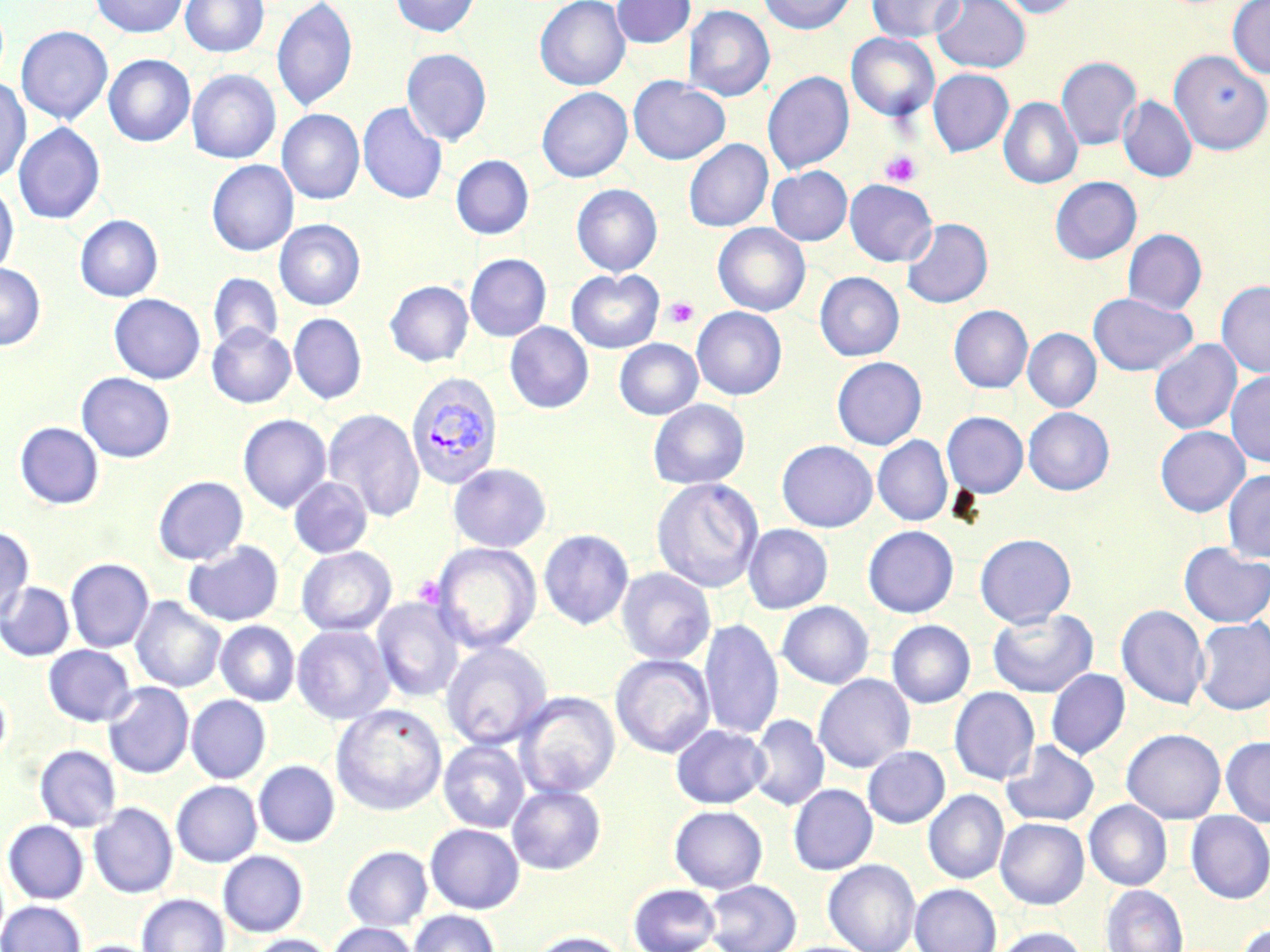

Summary:
  - Coordinate format: approximate bounding boxes as (x1, y1, x2, y2) in pixels
  - Uninfected red blood cell locations: (89, 0, 188, 37), (180, 0, 269, 57), (271, 0, 358, 113), (391, 0, 481, 37), (534, 0, 630, 90), (611, 0, 696, 48), (757, 0, 856, 34), (867, 0, 965, 43), (932, 0, 1031, 73), (996, 0, 1084, 18), (1227, 0, 1270, 78), (683, 5, 775, 102), (15, 25, 113, 124), (846, 32, 939, 121), (401, 48, 492, 146), (1170, 51, 1269, 155), (104, 54, 195, 146), (1056, 57, 1141, 150), (928, 68, 1014, 156), (188, 70, 280, 163), (195, 71, 287, 255), (762, 71, 854, 174), (0, 77, 31, 184), (628, 77, 730, 165), (536, 87, 632, 182), (1118, 96, 1197, 182), (998, 97, 1083, 189), (358, 101, 447, 205), (277, 109, 364, 204), (13, 122, 105, 224), (683, 139, 773, 232), (451, 155, 534, 239), (206, 160, 298, 256), (767, 166, 852, 245), (1050, 177, 1141, 264), (844, 179, 938, 267), (0, 183, 19, 275), (571, 184, 662, 276), (75, 215, 163, 302), (901, 218, 993, 308), (274, 219, 366, 310), (713, 223, 810, 316), (1122, 229, 1207, 315), (465, 253, 551, 341), (0, 263, 45, 350), (566, 269, 664, 353), (815, 272, 904, 361), (208, 273, 283, 351), (385, 280, 473, 367), (1216, 280, 1270, 378), (1088, 293, 1197, 376), (109, 294, 205, 384), (948, 305, 1033, 393), (692, 307, 787, 399), (288, 313, 367, 405), (505, 322, 593, 414), (207, 324, 296, 408), (1022, 328, 1101, 412), (614, 339, 703, 420), (1149, 339, 1242, 435), (831, 357, 926, 450), (1226, 371, 1270, 467), (76, 372, 175, 462), (648, 399, 750, 489), (1023, 407, 1115, 495), (322, 408, 424, 522), (942, 411, 1028, 498), (238, 414, 331, 513), (15, 421, 103, 509), (1155, 426, 1249, 517), (873, 436, 953, 526), (776, 440, 878, 532), (448, 463, 551, 552), (1222, 469, 1270, 562), (153, 475, 249, 565), (289, 477, 373, 558), (651, 478, 763, 594), (743, 524, 833, 614), (0, 525, 34, 622), (863, 525, 959, 618), (538, 529, 634, 630), (975, 533, 1076, 628), (182, 541, 284, 626), (432, 542, 541, 653), (1179, 542, 1270, 627), (296, 546, 396, 636), (66, 558, 154, 652), (616, 567, 715, 665), (0, 582, 74, 661), (130, 596, 226, 693), (372, 597, 466, 702), (777, 601, 874, 689), (1116, 604, 1209, 710), (987, 608, 1098, 697), (1194, 616, 1270, 715), (698, 618, 783, 739), (887, 620, 975, 708), (215, 621, 300, 706), (292, 625, 394, 724), (441, 641, 553, 750), (43, 645, 136, 726), (610, 654, 714, 758), (1046, 669, 1130, 759), (813, 674, 915, 772), (0, 681, 11, 769), (103, 682, 194, 779), (949, 687, 1040, 785), (514, 691, 620, 798), (186, 695, 271, 784), (331, 703, 448, 815), (748, 714, 829, 811), (671, 724, 769, 808), (1122, 728, 1225, 823), (1221, 736, 1270, 827), (439, 740, 530, 833), (1001, 740, 1099, 827), (34, 745, 121, 832), (863, 746, 950, 828), (253, 760, 339, 847), (171, 780, 262, 867), (788, 783, 877, 875), (507, 784, 606, 875), (923, 790, 1009, 884), (1084, 800, 1172, 890), (89, 803, 177, 898), (669, 805, 767, 893), (1186, 811, 1270, 903), (995, 818, 1089, 909), (3, 820, 89, 904), (425, 823, 524, 913), (342, 845, 432, 931), (218, 850, 308, 937), (823, 859, 921, 952), (704, 879, 802, 952), (909, 883, 1002, 952), (628, 884, 722, 952), (1101, 885, 1188, 952), (137, 894, 230, 952), (0, 899, 87, 952), (409, 910, 500, 952), (327, 922, 419, 952), (1236, 923, 1270, 952), (991, 926, 1089, 952), (527, 931, 629, 952), (243, 933, 336, 952), (70, 940, 161, 952)
  - Plasmodium vivax-infected red blood cell locations: (405, 371, 504, 490)
  - Platelet locations: (879, 149, 922, 187), (663, 297, 700, 329)
  - Slide-level diagnosis: Plasmodium vivax
  - Stain: May-Grünwald-Giemsa
  - Modality: light microscopy
  - Field of view: one of a larger specimen
  - Image size: 1270×952 pixels
  - Preparation: thin blood smear
  - Magnification: 1000x